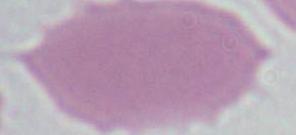

{
  "magnification": "1000x",
  "modality": "photomicrograph",
  "identification": "erythrocyte"
}